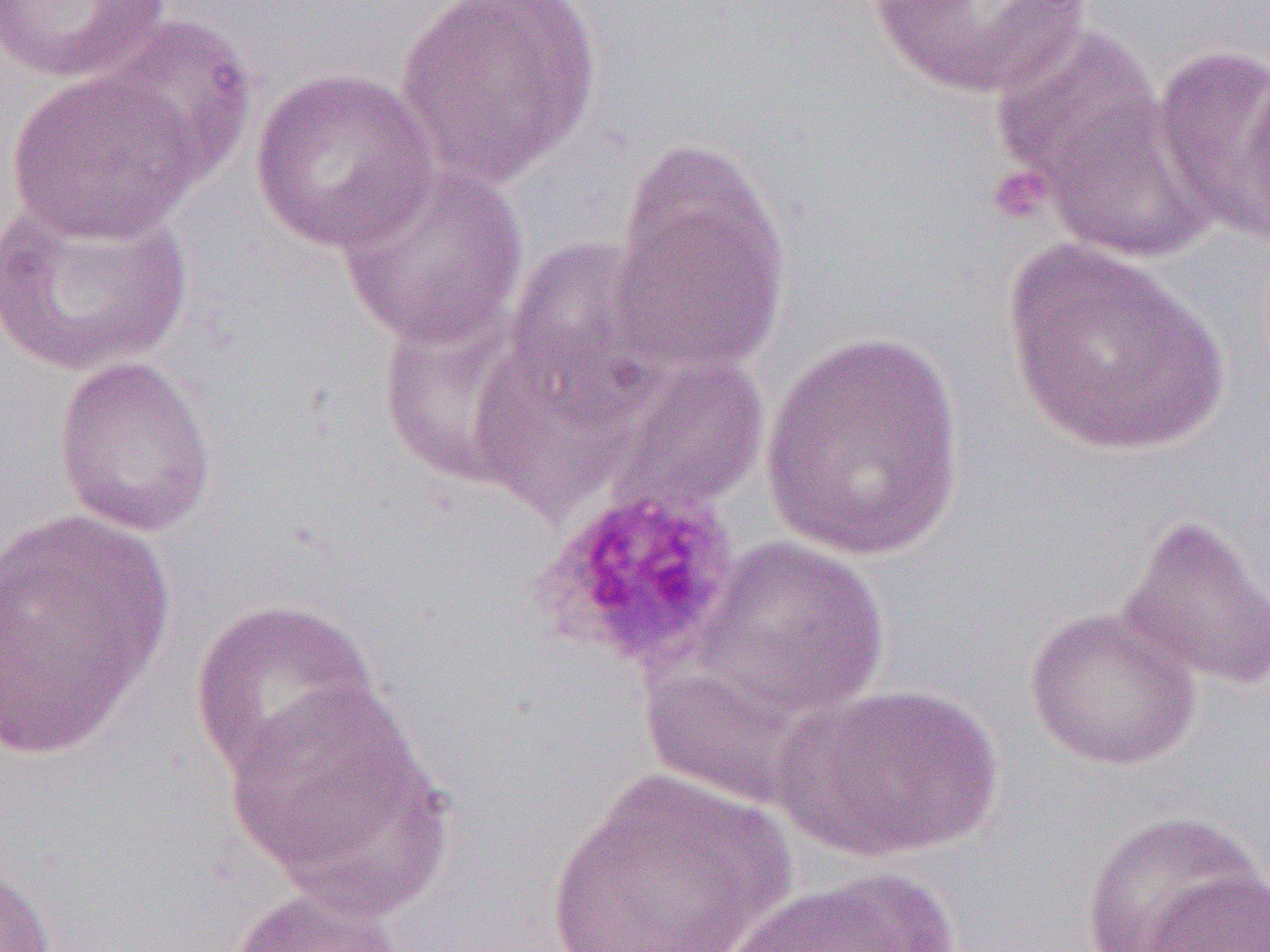

{
  "slide_level_diagnosis": "Plasmodium ovale",
  "image_size": "1270×952 pixels",
  "uninfected_red_blood_cell_locations": "approximate bounding boxes as (x1,y1)-(x2,y2) corner pairs in pixels: (0,0)-(172,83), (394,0)-(602,186), (865,0)-(1091,102), (97,14)-(257,187), (988,22)-(1172,212), (1152,43)-(1270,245), (7,68)-(203,244), (249,68)-(439,255), (1027,85)-(1215,265), (608,143)-(792,378), (333,160)-(529,351), (0,191)-(195,378), (501,236)-(674,414), (1003,239)-(1229,457), (759,330)-(969,562), (468,341)-(642,520), (594,350)-(770,517), (52,354)-(219,538), (0,509)-(176,761), (1116,512)-(1270,694), (684,535)-(891,728), (188,597)-(383,784), (1024,605)-(1203,771), (222,679)-(448,907), (772,684)-(1002,861), (542,767)-(800,952), (1078,810)-(1267,952), (0,859)-(57,952), (711,867)-(969,952), (1143,868)-(1270,951), (225,885)-(410,952)",
  "field_of_view": "one of a larger specimen",
  "platelet_locations": "approximate bounding boxes as (x1,y1)-(x2,y2) corner pairs in pixels: (986,168)-(1050,225), (539,485)-(743,672)",
  "modality": "optical microscopy",
  "preparation": "thin blood smear",
  "magnification": "1000x"
}